Locate every blood parasite and identify its species.
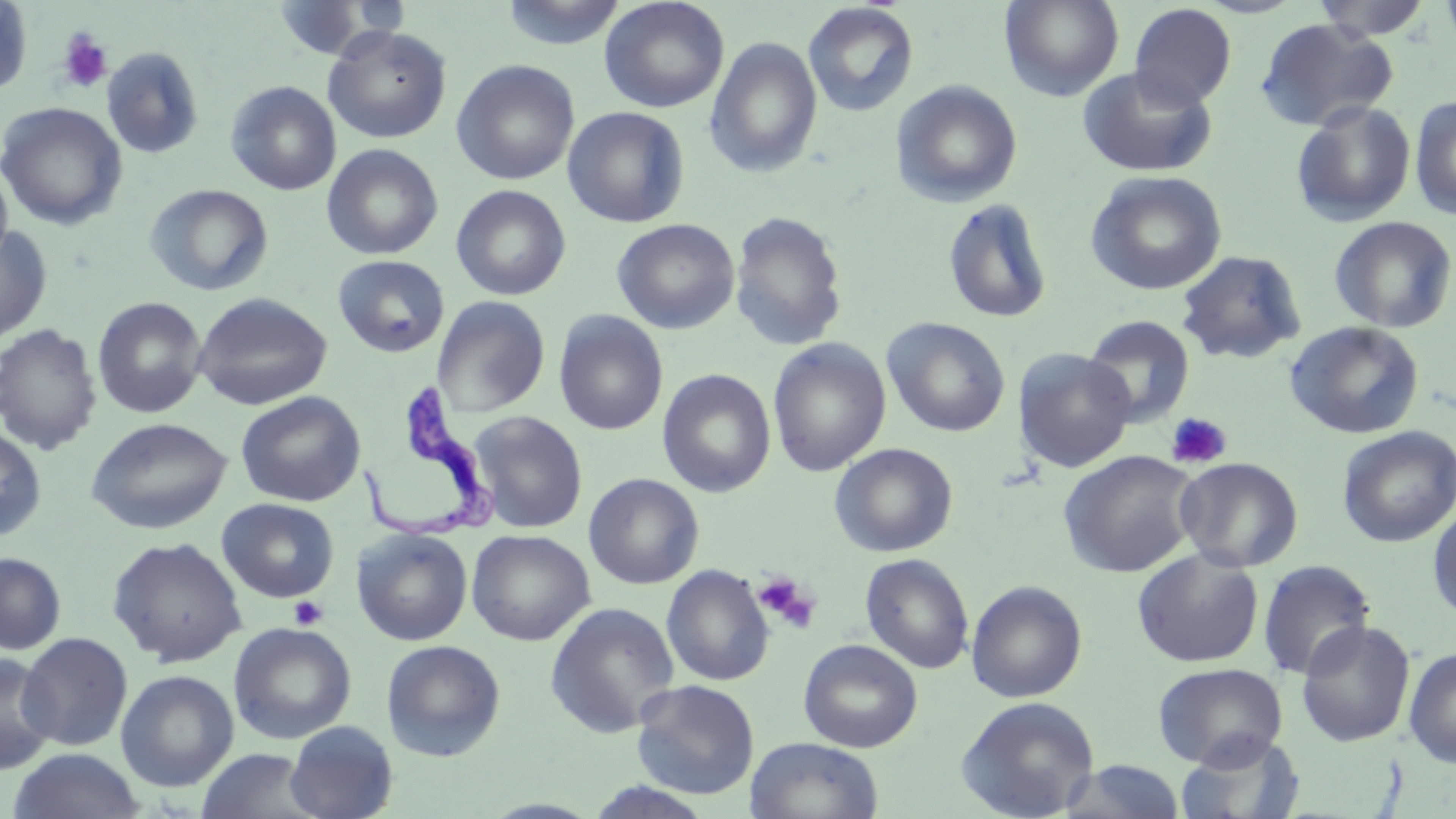
Approximate bounding boxes as (x1, y1, x2, y2) in pixels.
Trypanosoma brucei: (358, 381, 503, 543).
No Plasmodium falciparum, Plasmodium ovale, Plasmodium malariae, Plasmodium vivax, or Babesia divergens observed.

Summary:
  - Uninfected red blood cell locations: (0, 0, 33, 96), (498, 0, 628, 49), (599, 0, 729, 113), (999, 0, 1124, 101), (1311, 0, 1433, 41), (1438, 0, 1456, 55), (272, 1, 380, 60), (802, 3, 919, 117), (1129, 3, 1237, 110), (1255, 18, 1397, 132), (323, 25, 452, 144), (705, 36, 823, 178), (101, 46, 204, 160), (451, 60, 580, 185), (1077, 66, 1218, 178), (225, 80, 341, 196), (892, 80, 1023, 208), (1410, 95, 1456, 221), (1291, 100, 1417, 227), (0, 102, 127, 230), (562, 106, 690, 228), (322, 143, 444, 260), (0, 163, 14, 271), (1085, 171, 1227, 296), (144, 183, 274, 297), (451, 184, 571, 301), (942, 197, 1054, 324), (728, 211, 848, 351), (1329, 216, 1455, 334), (612, 218, 739, 334), (0, 224, 53, 344), (1176, 250, 1307, 364), (332, 254, 450, 358), (191, 292, 332, 411), (92, 296, 208, 419), (432, 296, 551, 417), (554, 311, 668, 436), (1082, 315, 1195, 429), (882, 317, 1011, 437), (1284, 321, 1424, 440), (0, 323, 103, 456), (768, 338, 891, 477), (1014, 348, 1137, 473), (658, 369, 776, 497), (236, 390, 366, 507), (467, 410, 588, 533), (86, 417, 232, 535), (1337, 425, 1456, 548), (0, 426, 47, 543), (829, 443, 958, 557), (1058, 450, 1202, 578), (1174, 456, 1303, 572), (583, 473, 704, 590), (217, 497, 340, 603), (1427, 502, 1456, 620), (352, 528, 473, 645), (466, 528, 595, 646), (107, 536, 247, 667), (1132, 548, 1264, 668), (0, 552, 66, 654), (860, 552, 974, 674), (1257, 560, 1376, 681), (661, 564, 775, 686), (966, 579, 1087, 703), (544, 602, 681, 738), (1296, 619, 1416, 748), (228, 622, 356, 744), (18, 632, 133, 751), (798, 638, 923, 753), (381, 639, 506, 762), (1403, 646, 1456, 768), (1, 653, 58, 775), (1151, 662, 1288, 769), (115, 669, 239, 792), (631, 679, 760, 800), (956, 696, 1100, 819), (284, 720, 398, 819), (1175, 733, 1304, 819), (746, 737, 884, 819), (8, 748, 144, 819), (195, 748, 323, 819), (1062, 760, 1186, 818)
  - Platelet locations: (57, 30, 112, 94), (1165, 411, 1232, 470), (753, 573, 820, 634), (289, 596, 328, 629)
  - Slide-level diagnosis: Trypanosoma brucei
  - Field of view: single
  - Stain: May-Grünwald-Giemsa
  - Preparation: thin blood smear
  - Image size: 1456×819 pixels
  - Magnification: 1000x
  - Modality: optical microscopy